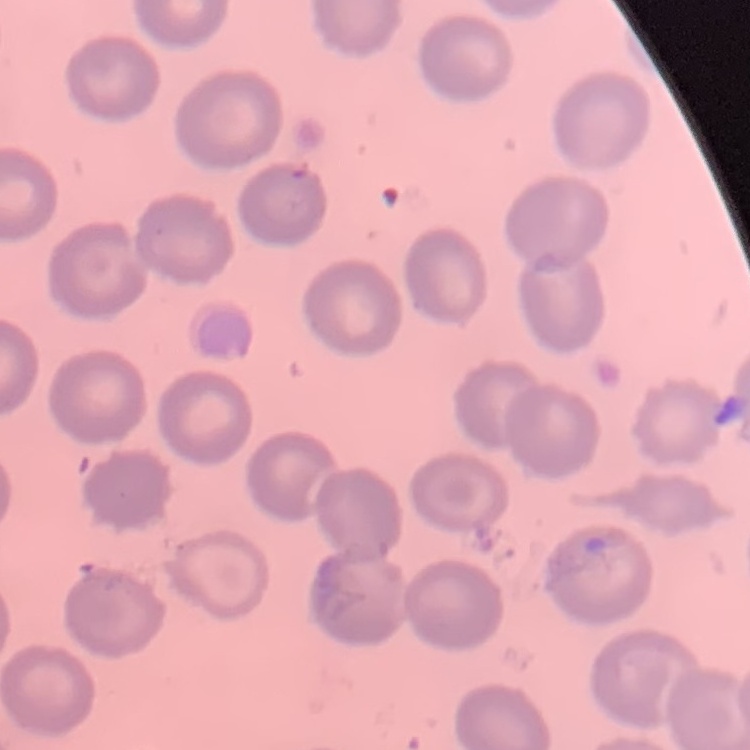

Summary:
  - Erythrocyte morphology: no rouleaux formation
  - Stain: Field's or Giemsa
  - Image type: one tile cut from a larger photomicrograph
  - Preparation: thin blood film